Identify the blood parasite species.
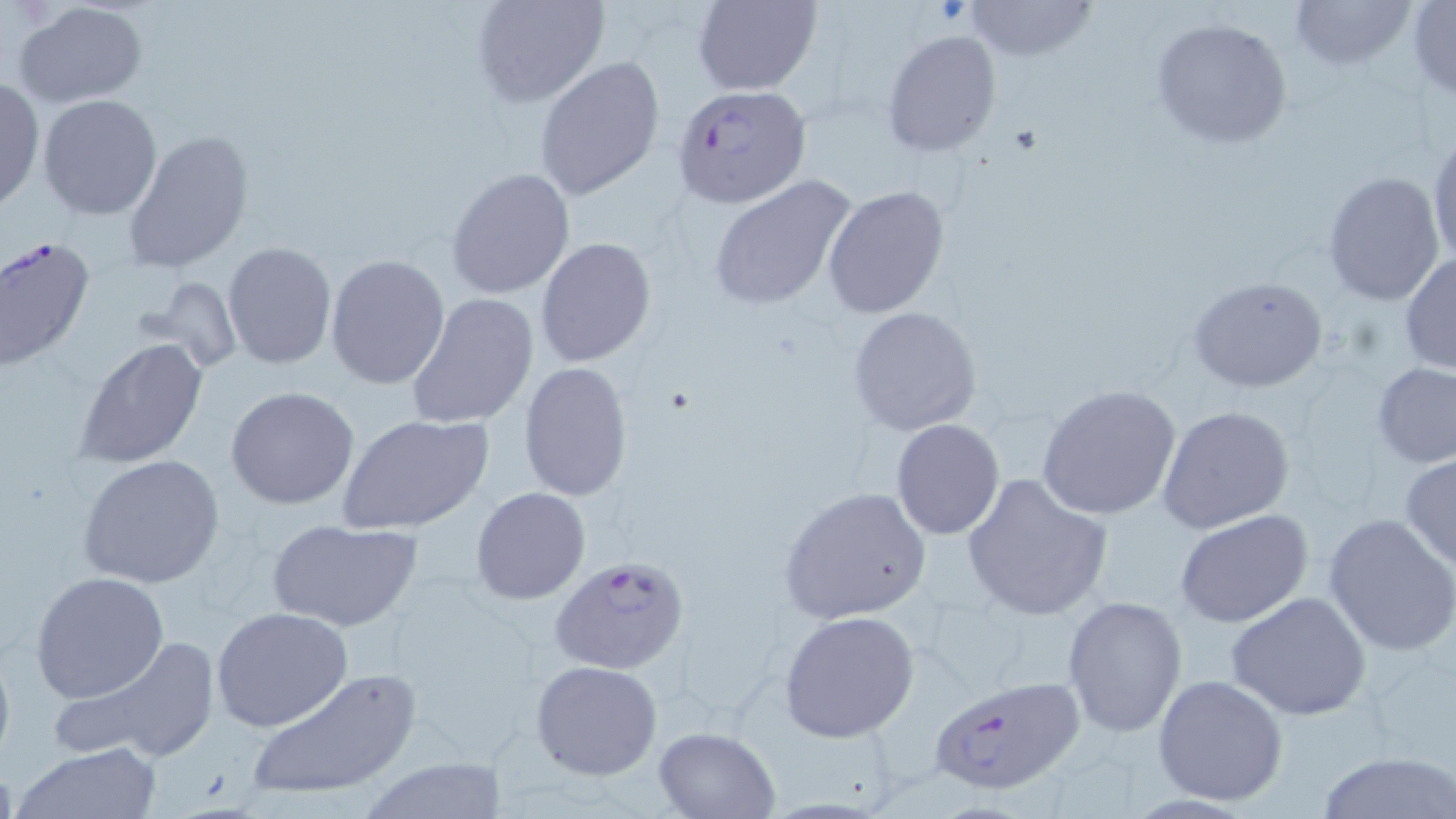
Plasmodium falciparum.

Summary:
  - Coordinate format: approximate bounding boxes as (x1,y1)-(x2,y2) corner pairs in pixels
  - Plasmodium falciparum-infected red blood cell locations: (674,85)-(811,210), (549,554)-(692,676), (927,672)-(1088,800)
  - Uninfected red blood cell locations: (468,0)-(610,108), (691,0)-(821,96), (962,0)-(1096,65), (1288,0)-(1416,74), (1406,1)-(1456,102), (12,2)-(150,110), (1150,15)-(1294,150), (882,29)-(1002,157), (535,57)-(665,201), (0,76)-(44,215), (38,95)-(163,221), (123,128)-(256,274), (1426,129)-(1456,275), (445,167)-(576,300), (1321,171)-(1446,306), (706,175)-(860,310), (824,186)-(952,319), (0,235)-(96,373), (535,238)-(656,368), (222,242)-(336,369), (1399,251)-(1456,376), (325,255)-(450,389), (1188,276)-(1329,394), (148,277)-(243,373), (406,293)-(537,431), (846,306)-(983,437), (74,336)-(208,470), (518,362)-(633,502), (1372,362)-(1456,469), (1036,384)-(1182,522), (225,385)-(360,509), (1156,405)-(1296,535), (340,415)-(494,537), (889,417)-(1006,541), (1400,453)-(1456,570), (79,455)-(226,590), (962,471)-(1112,621), (471,486)-(591,605), (777,486)-(933,624), (1174,510)-(1315,628), (1323,513)-(1456,656), (268,518)-(423,632), (29,571)-(170,704), (1226,591)-(1373,720), (1061,596)-(1188,739), (210,607)-(354,732), (780,610)-(920,742), (53,634)-(225,766), (0,636)-(15,774), (532,660)-(663,781), (243,668)-(423,804), (1153,673)-(1288,806), (651,726)-(779,818), (12,742)-(163,819), (1315,751)-(1454,819), (354,759)-(511,817)
  - Modality: optical microscopy
  - Stain: May-Grünwald-Giemsa
  - Preparation: thin blood smear
  - Image size: 1456×819 pixels
  - Field of view: one of a larger specimen
  - Magnification: 1000x